Assess for malaria.
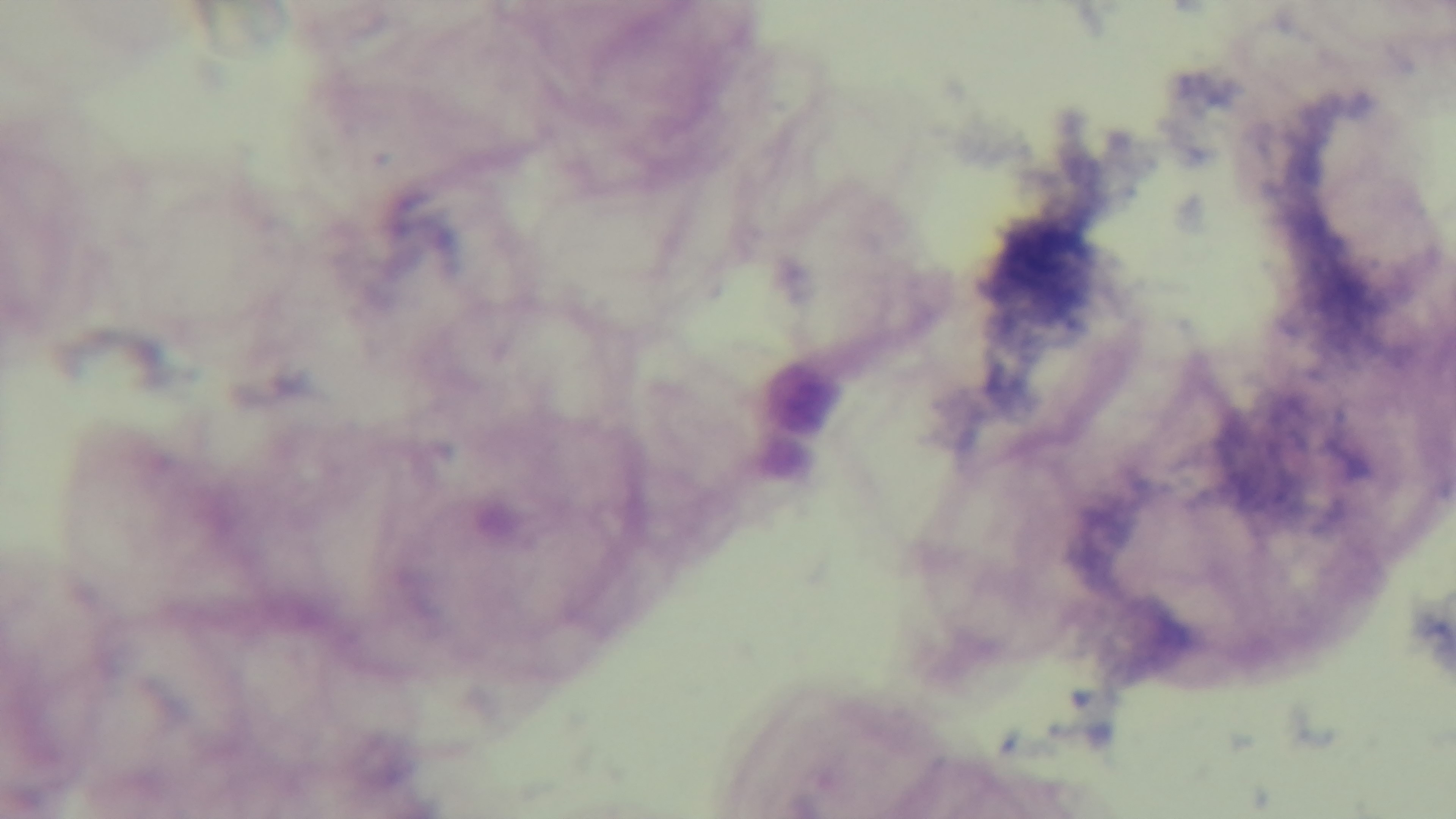
Negative.

{
  "capture": "mounted 4K digital camera",
  "modality": "light microscopy",
  "stain": "Giemsa",
  "objective": "100x oil immersion",
  "field_of_view": "single",
  "preparation": "thick blood film"
}